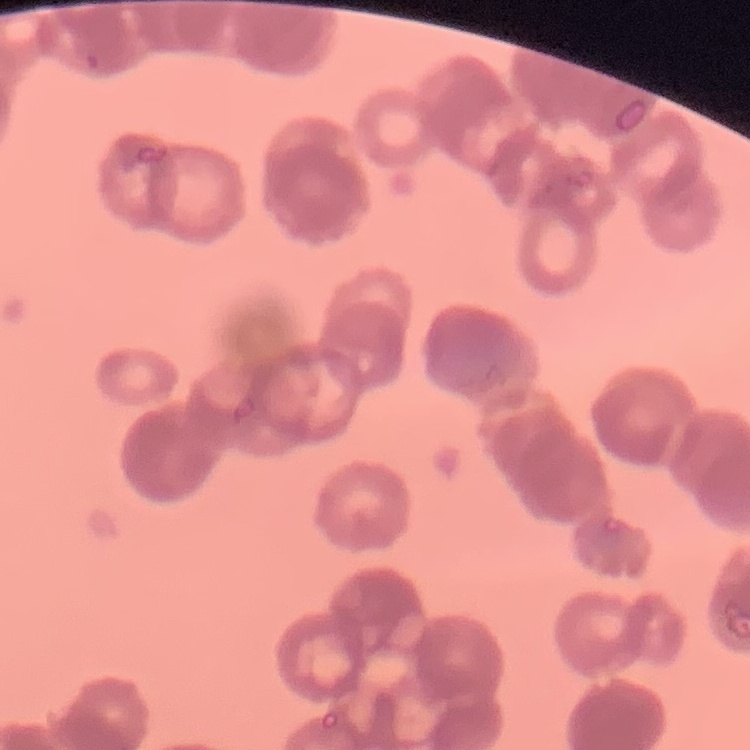
Summary:
  - Erythrocyte morphology: rouleaux formation
  - Stain: Field's or Giemsa
  - Preparation: thin blood smear
  - Image type: square crop of a larger photomicrograph